Point out each Plasmodium parasite.
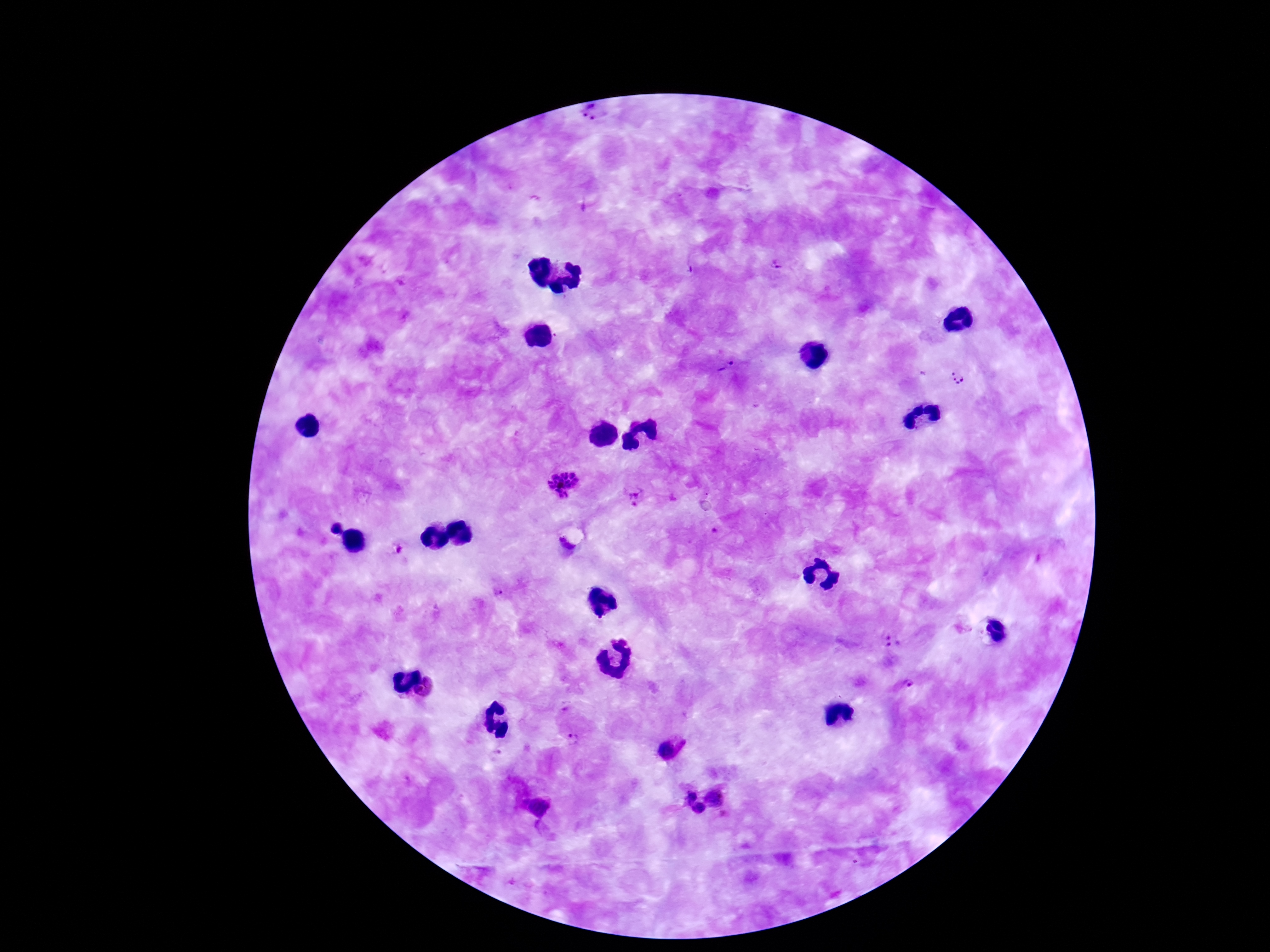
Approximate centers as [x, y] in pixels.
Plasmodium parasites: [592, 111], [776, 265], [726, 366], [959, 377], [563, 484], [639, 494], [334, 527], [499, 595], [890, 641], [907, 686], [426, 690], [575, 740], [690, 796], [718, 796], [538, 807], [698, 808].

Thick blood film. Image is 1270×952 pixels. Giemsa-stained preparation. One field from this slide. Smartphone photograph taken through the microscope eyepiece. 100x magnification. Patient malaria status: infected.